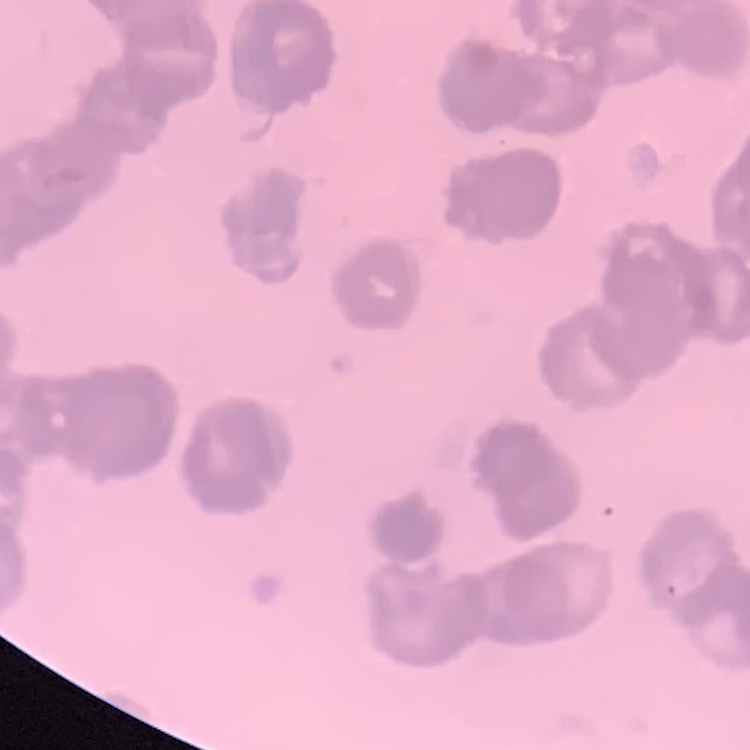

erythrocyte morphology = rouleaux formation
image type = square crop of a larger photomicrograph
preparation = thin peripheral smear
stain = Field's or Giemsa